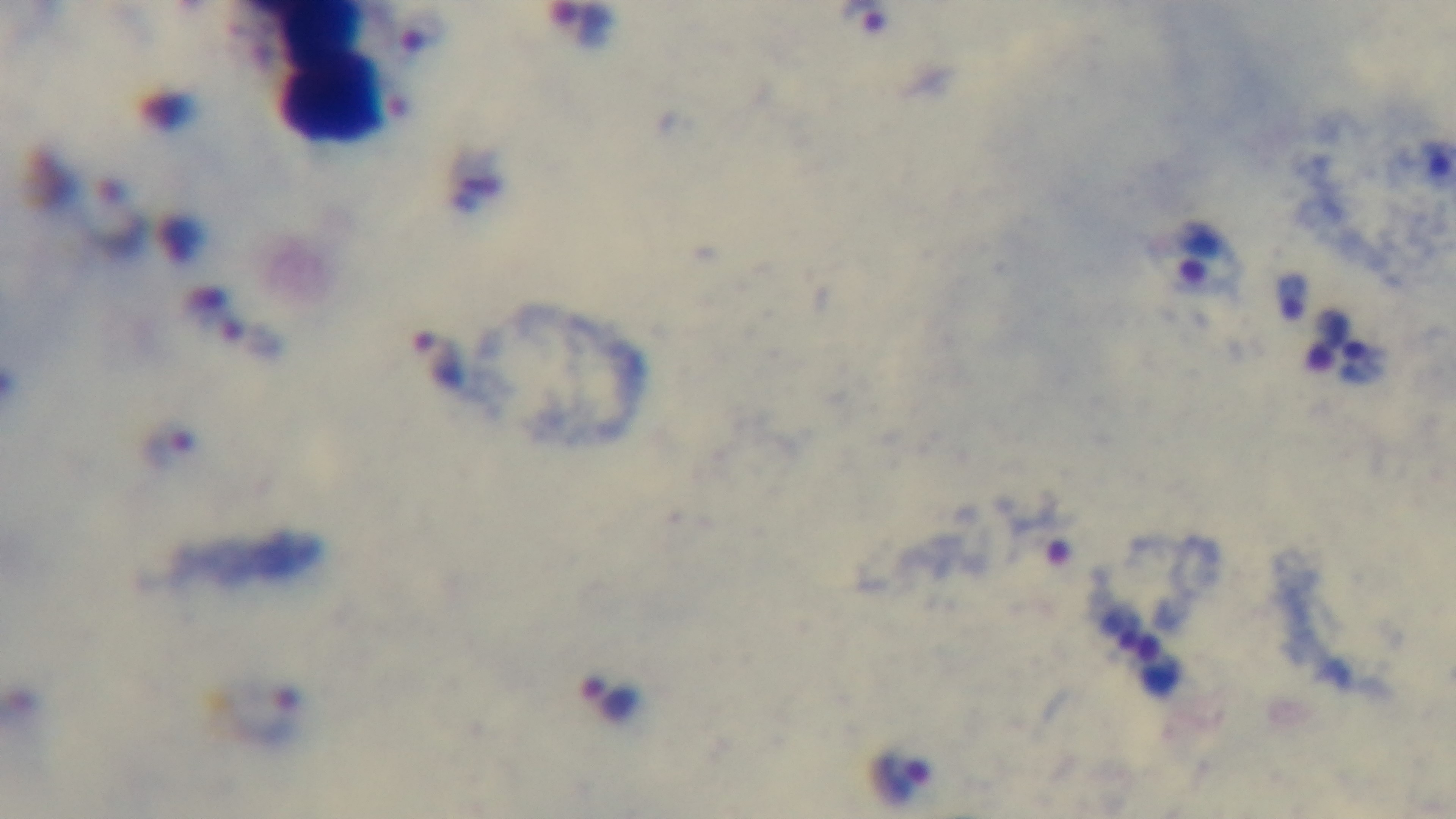

Preparation: thick blood film. 100x oil-immersion objective. Malaria status: infected. Mounted 4K digital camera. Light microscopy. Single field of view. Giemsa-stained.